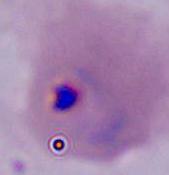
Summary:
  - Magnification: 400x or 1000x
  - Identification: Plasmodium
  - Modality: micrograph